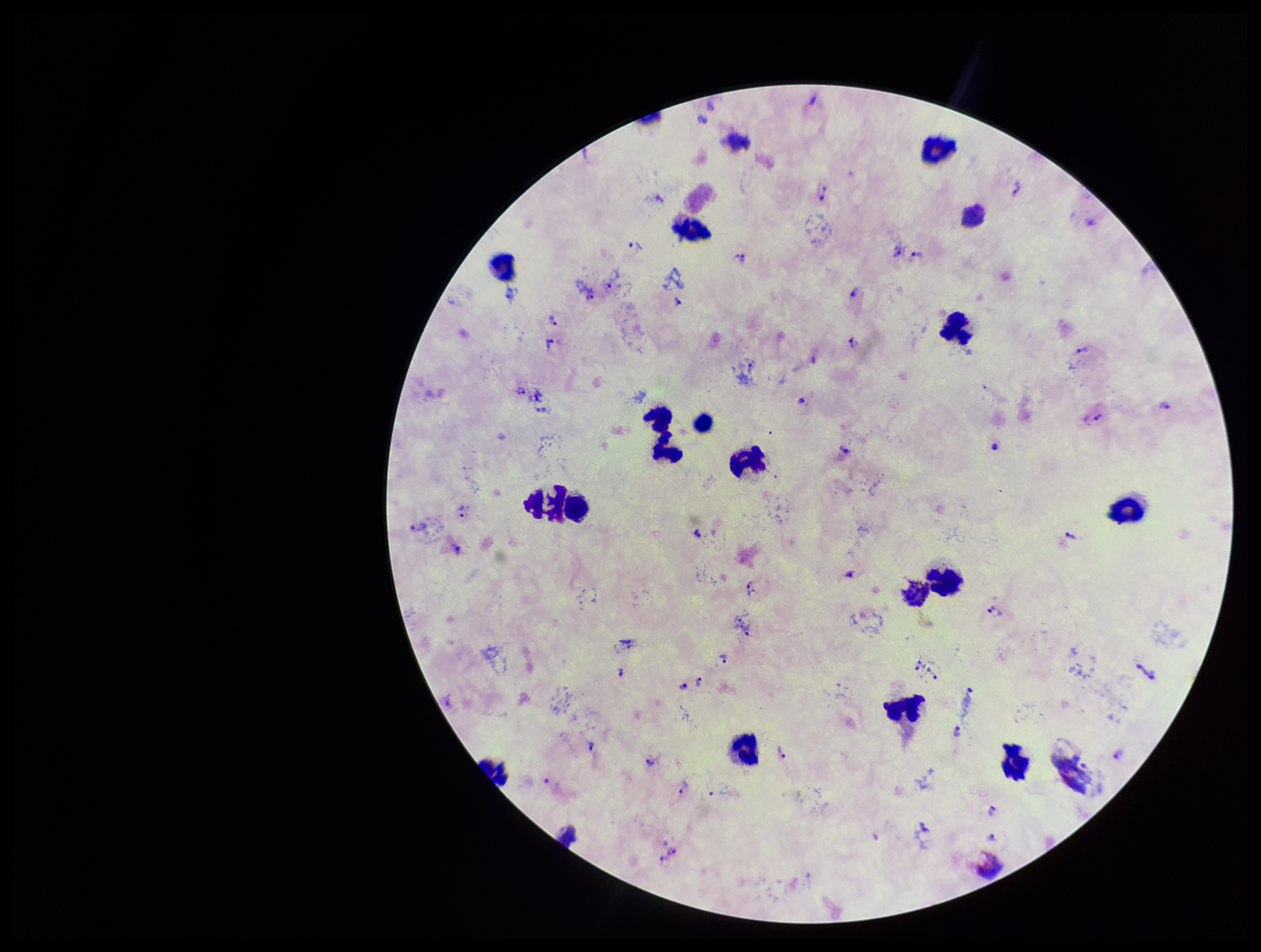

preparation = thick blood smear
parasite count = 50
leukocyte count = 19
image size = 1261×952 pixels
field of view = one from this slide
capture = smartphone photograph through the microscope eyepiece
Plasmodium parasites = seen
species reported for this patient = Plasmodium vivax
patient malaria status = infected
stain = Giemsa